Assess this cell for malaria.
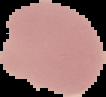

Uninfected.

{
  "image_size": "106×97 pixels",
  "image_type": "cell region segmented out of the field of view; surrounding area masked to black",
  "preparation": "thin blood smear"
}